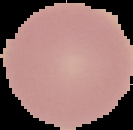

Segmented cell region on a black background. From a thin blood smear. Image is 133×130 pixels. Malaria status: uninfected.